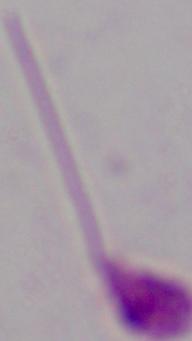

Micrograph. A Leishmania parasite is seen. 1000x magnification.